Locate platelets.
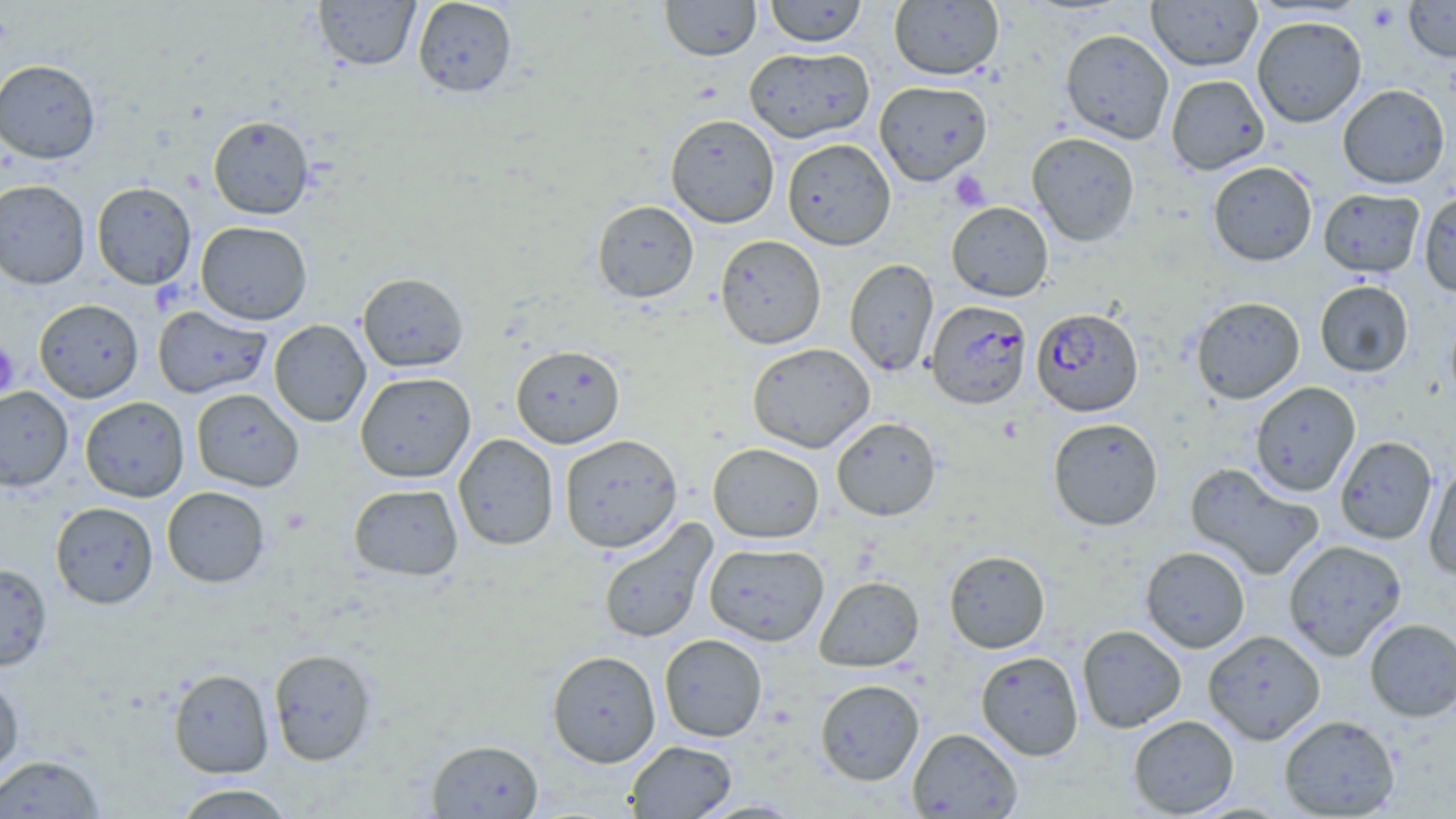

Approximate bounding boxes as (x1,y1)-(x2,y2) corner pairs in pixels.
Platelets: (1365,3)-(1402,32), (949,170)-(991,212), (0,343)-(19,397).

{
  "plasmodium_falciparum_infected_red_blood_cell_locations": "approximate bounding boxes as (x1,y1)-(x2,y2) corner pairs in pixels: (926,300)-(1032,410), (1031,307)-(1144,416)",
  "slide_level_diagnosis": "Plasmodium falciparum",
  "image_size": "1456×819 pixels",
  "modality": "optical microscopy",
  "field_of_view": "one of a larger specimen",
  "magnification": "1000x",
  "preparation": "thin blood film",
  "stain": "May-Grünwald-Giemsa",
  "uninfected_red_blood_cell_locations": "approximate bounding boxes as (x1,y1)-(x2,y2) corner pairs in pixels: (313,0)-(420,71), (412,0)-(518,98), (660,0)-(761,62), (764,0)-(868,47), (1146,0)-(1263,72), (1404,0)-(1456,62), (888,1)-(1004,80), (1251,16)-(1367,127), (1060,29)-(1174,144), (744,46)-(874,143), (0,59)-(101,164), (1166,74)-(1269,175), (874,80)-(993,185), (1337,84)-(1450,189), (665,114)-(780,228), (208,115)-(314,219), (1027,132)-(1140,246), (782,138)-(896,250), (1208,161)-(1317,266), (0,180)-(91,289), (91,181)-(197,290), (1318,188)-(1425,277), (1418,190)-(1456,298), (592,199)-(699,303), (946,202)-(1053,301), (196,221)-(312,325), (715,235)-(826,349), (845,258)-(939,377), (357,272)-(468,372), (1314,280)-(1414,377), (1191,296)-(1305,404), (34,299)-(144,402), (152,305)-(272,399), (1445,306)-(1456,411), (269,320)-(371,427), (747,342)-(875,452), (510,344)-(625,448), (355,371)-(476,482), (1249,381)-(1360,497), (0,386)-(73,492), (191,388)-(304,492), (80,396)-(189,502), (831,416)-(942,521), (1047,418)-(1163,531), (453,433)-(559,550), (559,434)-(683,552), (1335,435)-(1438,544), (708,443)-(824,543), (1423,462)-(1456,580), (1185,463)-(1325,580), (348,483)-(464,580), (162,486)-(270,588), (50,502)-(158,609), (597,518)-(716,645), (1282,539)-(1407,660), (704,542)-(829,646), (1140,546)-(1250,653), (944,550)-(1050,653), (0,562)-(52,671), (815,576)-(924,671), (1364,618)-(1456,722), (1076,625)-(1187,733), (1202,630)-(1326,744), (659,634)-(768,741), (268,648)-(377,766), (547,650)-(661,767), (976,651)-(1084,760), (168,668)-(274,778), (0,673)-(24,780), (815,679)-(925,785), (1279,714)-(1400,818), (1128,715)-(1239,817), (908,728)-(1023,817), (426,739)-(544,818), (625,739)-(737,818), (1,754)-(105,818), (172,783)-(297,818), (695,800)-(807,818)"
}